State which parasite is depicted.
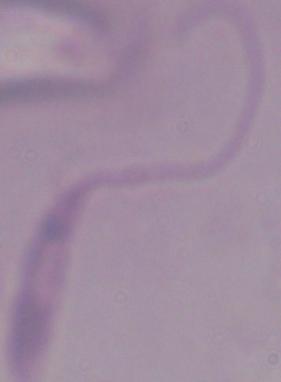
This is Leishmania.

modality = micrograph
magnification = 1000x